Comment on the morphology of the red blood cells.
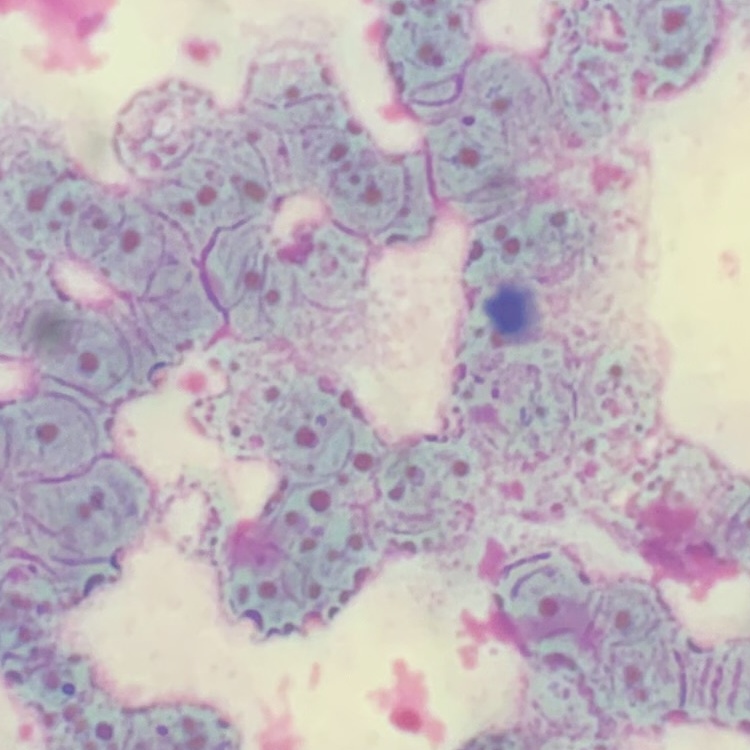
They show rouleaux formation.

Thin blood film. Field's or Giemsa stain. One tile cut from a larger photomicrograph.